Assess this cell for malaria.
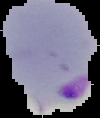

Parasitized.

Cell region segmented out of the field of view; the surrounding area is masked to black. From a thin blood film. Image is 100×118 pixels.